Evaluate for Plasmodium parasites.
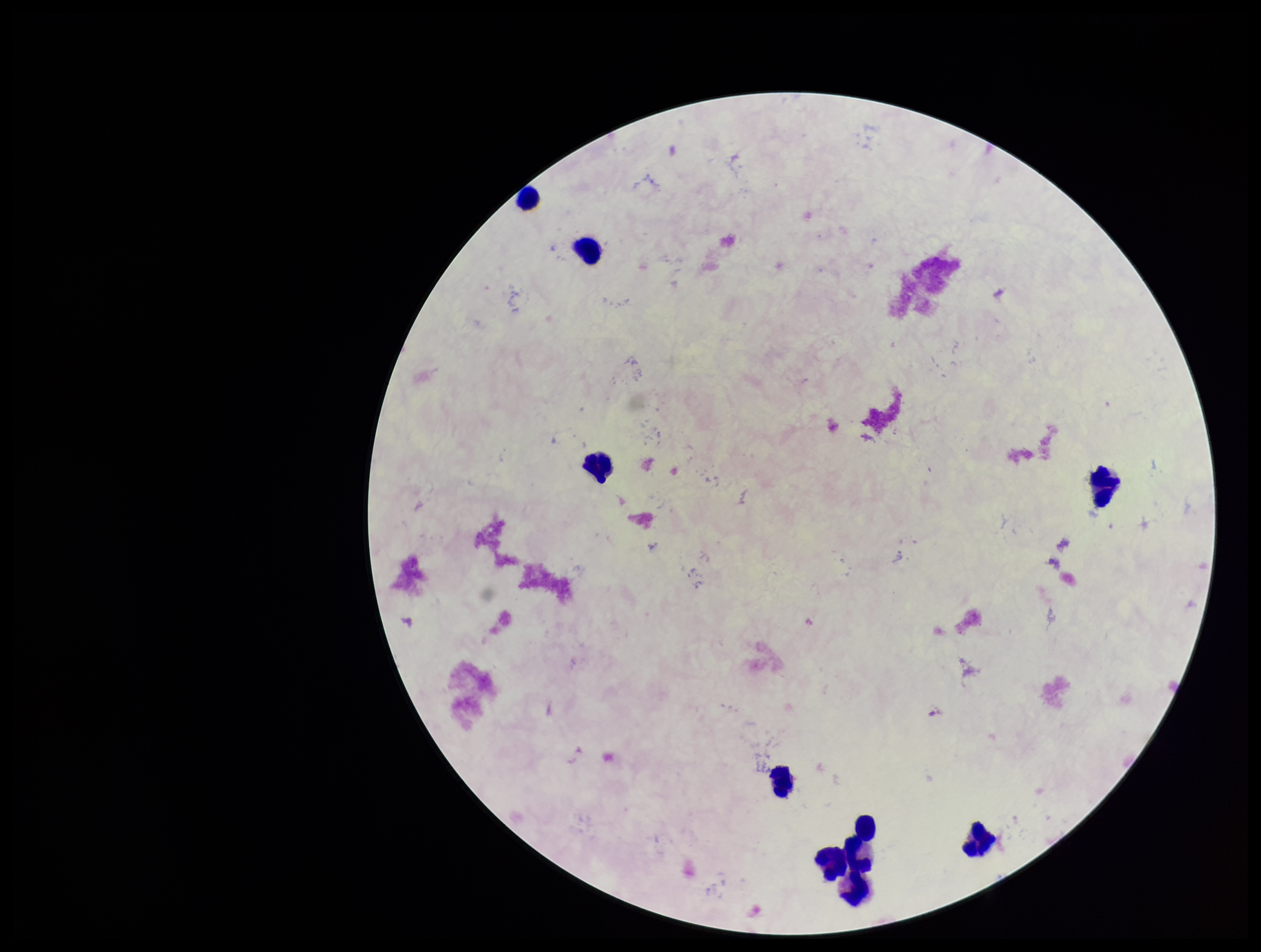
None seen.

Patient malaria status: negative. Giemsa stain. Parasite count: 0. Single field of view. Photographed through the microscope eyepiece with a smartphone camera. Image is 1261×952 pixels. Leukocyte count: 9. Preparation: thick blood smear.